Name the parasite shown.
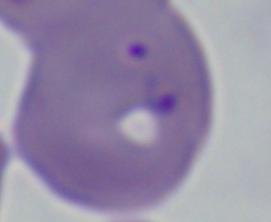

This is Babesia.

Summary:
  - Magnification: 1000x
  - Modality: micrograph